Classify this cell by malaria status.
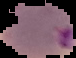

Parasitized.

image size = 76×58 pixels
image type = segmented cell region on a black background
preparation = thin blood smear